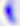

magnification = 400x
identification = Toxoplasma gondii
modality = micrograph